Report the malaria status.
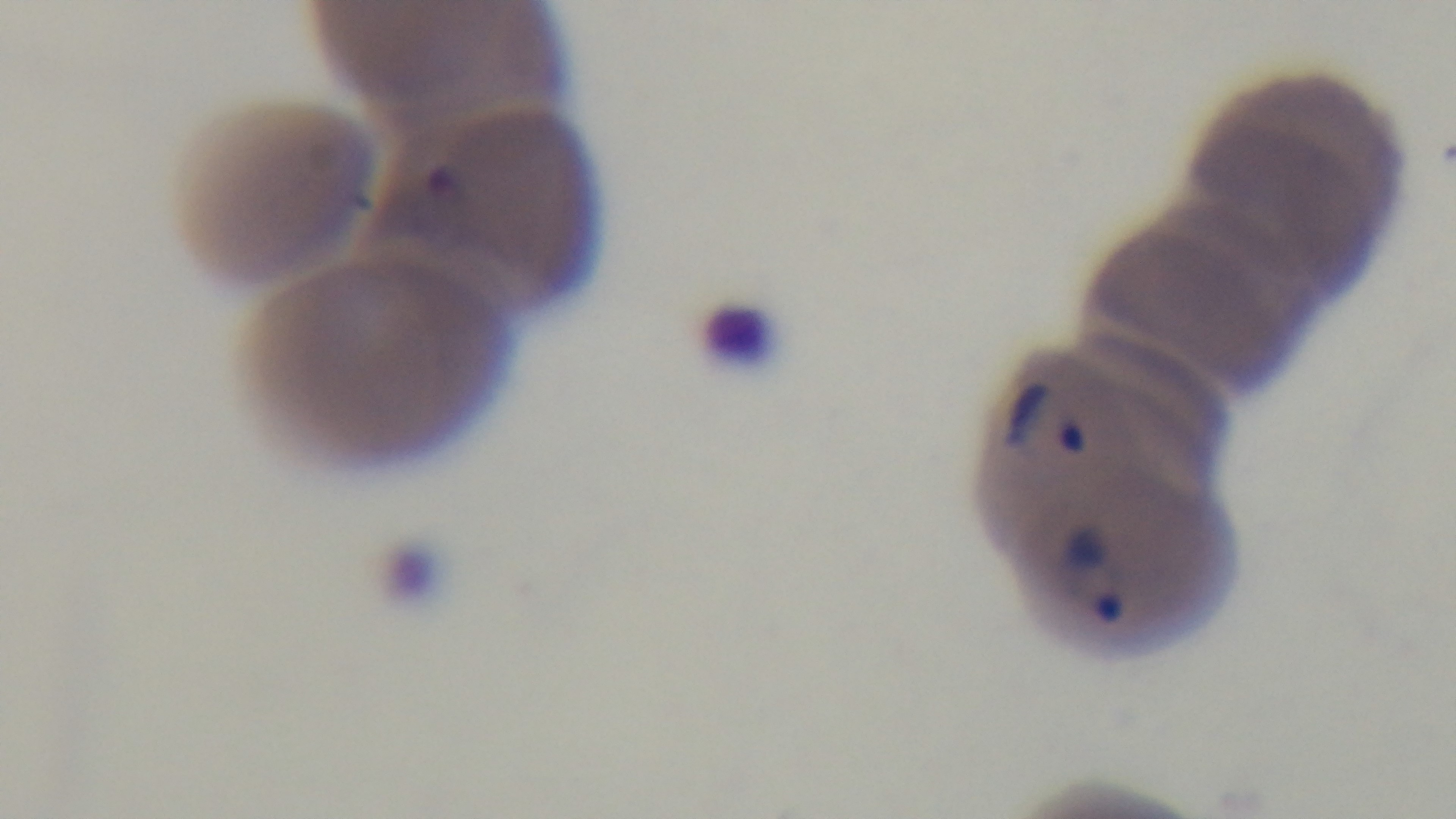
It is infected.

modality = light microscopy
preparation = thin
objective = 100x oil immersion
capture = mounted 4K digital camera
stain = Giemsa
field of view = single